Comment on the morphology of the red blood cells.
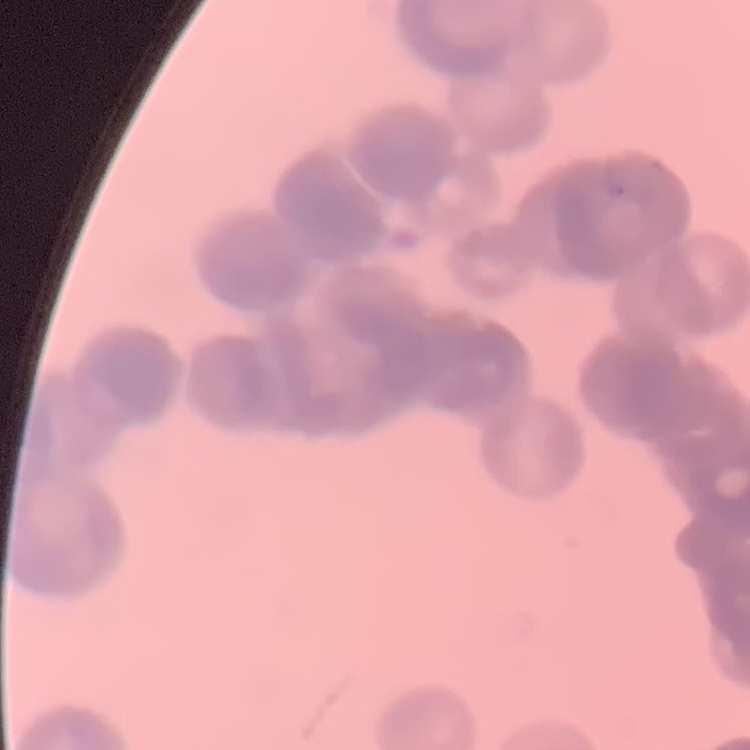

They show rouleaux formation.

image type = one tile cut from a larger photomicrograph
preparation = thin blood film
stain = Field's or Giemsa